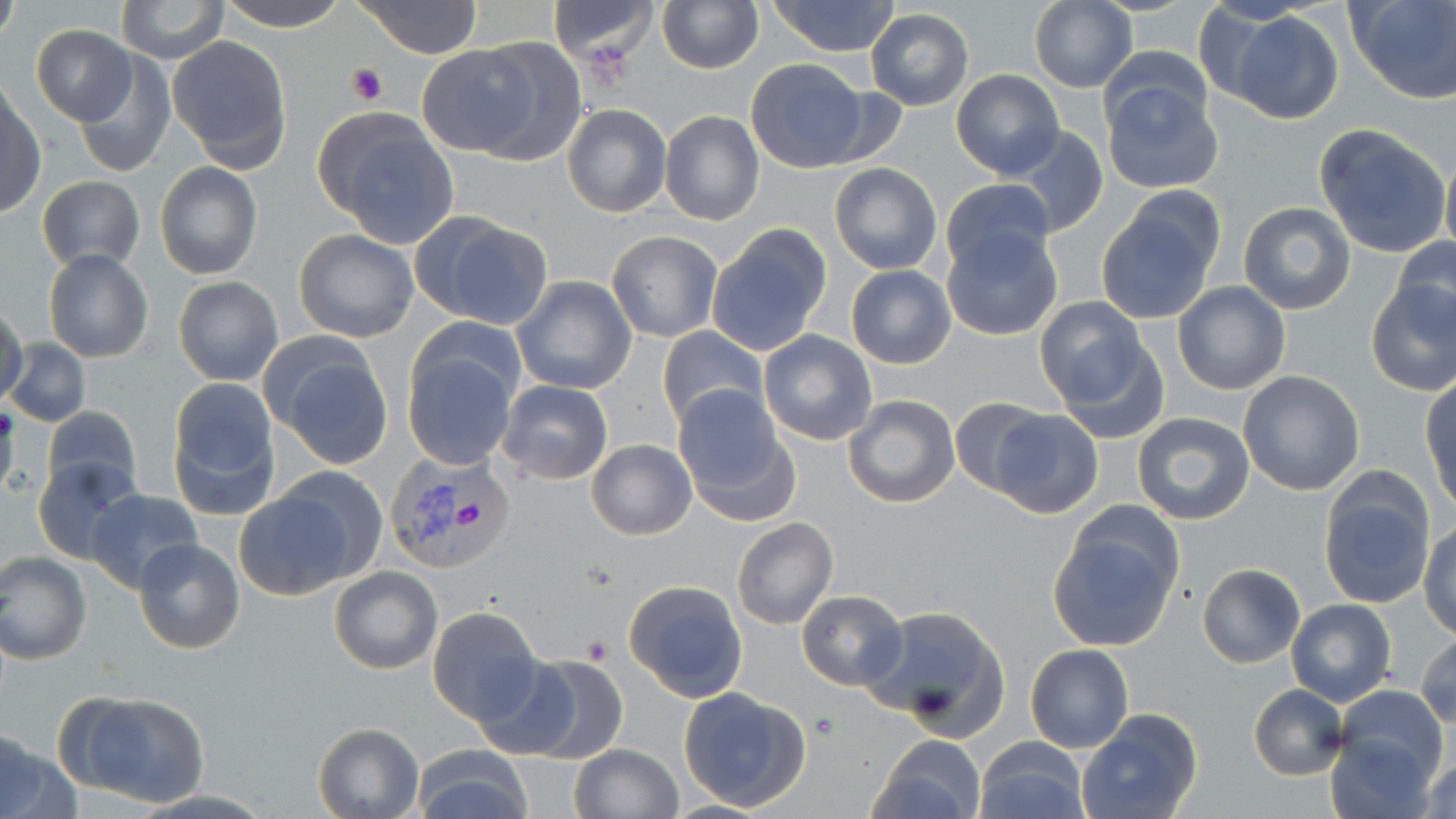

slide_level_diagnosis: Plasmodium vivax
uninfected_red_blood_cell_locations: 'approximate bounding boxes as (x1,y1)-(x2,y2) corner pairs in pixels: (217,0)-(351,30), (355,0)-(481,58), (656,0)-(763,74), (1189,0)-(1293,110), (1346,0)-(1454,104), (116,1)-(228,63), (547,1)-(659,62), (766,1)-(902,56), (1028,1)-(1139,93), (1,3)-(18,49), (866,8)-(975,111), (1226,11)-(1344,123), (32,25)-(136,124), (166,36)-(291,170), (471,37)-(588,168), (416,43)-(550,159), (1102,43)-(1213,135), (73,53)-(176,178), (744,57)-(874,172), (951,69)-(1064,179), (1100,83)-(1224,194), (1,93)-(46,218), (562,102)-(672,218), (659,110)-(765,226), (313,111)-(461,248), (1311,123)-(1450,258), (1011,125)-(1108,237), (1440,152)-(1456,262), (830,162)-(942,274), (154,163)-(262,279), (36,176)-(146,271), (941,177)-(1054,275), (1095,199)-(1222,325), (1238,201)-(1357,315), (421,214)-(553,329), (706,224)-(832,357), (941,228)-(1064,342), (294,229)-(420,344), (606,231)-(724,342), (1394,236)-(1456,334), (43,248)-(153,364), (845,264)-(957,369), (511,274)-(638,397), (173,276)-(283,385), (1366,278)-(1456,398), (1172,282)-(1291,397), (1034,295)-(1155,416), (0,305)-(25,405), (657,325)-(768,428), (757,329)-(879,445), (5,338)-(91,427), (263,339)-(395,467), (403,342)-(519,471), (1238,371)-(1365,495), (1422,378)-(1455,510), (167,380)-(281,519), (497,381)-(614,485), (673,387)-(793,519), (843,395)-(961,509), (951,397)-(1056,497), (0,403)-(18,503), (42,404)-(142,498), (986,410)-(1102,521), (1132,412)-(1257,526), (587,438)-(697,540), (33,455)-(142,564), (272,465)-(388,581), (1317,471)-(1436,611), (86,490)-(202,594), (233,492)-(354,599), (732,517)-(838,630), (1047,521)-(1179,654), (1421,521)-(1456,638), (133,539)-(245,654), (0,550)-(93,665), (1198,563)-(1305,667), (330,566)-(442,675), (623,580)-(750,700), (796,589)-(906,691), (1286,599)-(1395,707), (860,604)-(1011,737), (426,607)-(541,723), (1415,632)-(1456,728), (1024,643)-(1133,753), (518,654)-(629,766), (470,655)-(585,761), (1247,684)-(1348,780), (678,685)-(811,813), (1333,686)-(1449,788), (59,688)-(213,810), (1077,709)-(1201,819), (313,722)-(424,818), (1326,733)-(1437,819), (867,734)-(985,819), (0,735)-(78,819), (976,735)-(1088,819), (569,744)-(683,819), (412,746)-(534,819), (1420,754)-(1456,819)'
preparation: thin blood film
platelet_locations: 'approximate bounding boxes as (x1,y1)-(x2,y2) corner pairs in pixels: (347,63)-(387,106), (581,634)-(614,663)'
modality: optical microscopy
plasmodium_vivax_infected_red_blood_cell_locations: 'approximate bounding boxes as (x1,y1)-(x2,y2) corner pairs in pixels: (385,450)-(518,575)'
stain: May-Grünwald-Giemsa
image_size: 1456×819 pixels
magnification: 1000x
field_of_view: one of a larger specimen